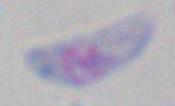
magnification: 1000x
modality: micrograph
identification: Toxoplasma gondii